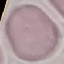
Malaria status: uninfected. Thin blood film. Giemsa-stained preparation. Automatically extracted cell patch, resized to 64 × 64 pixels. Acquired by smartphone through the microscope eyepiece.